Point out each leukocyte.
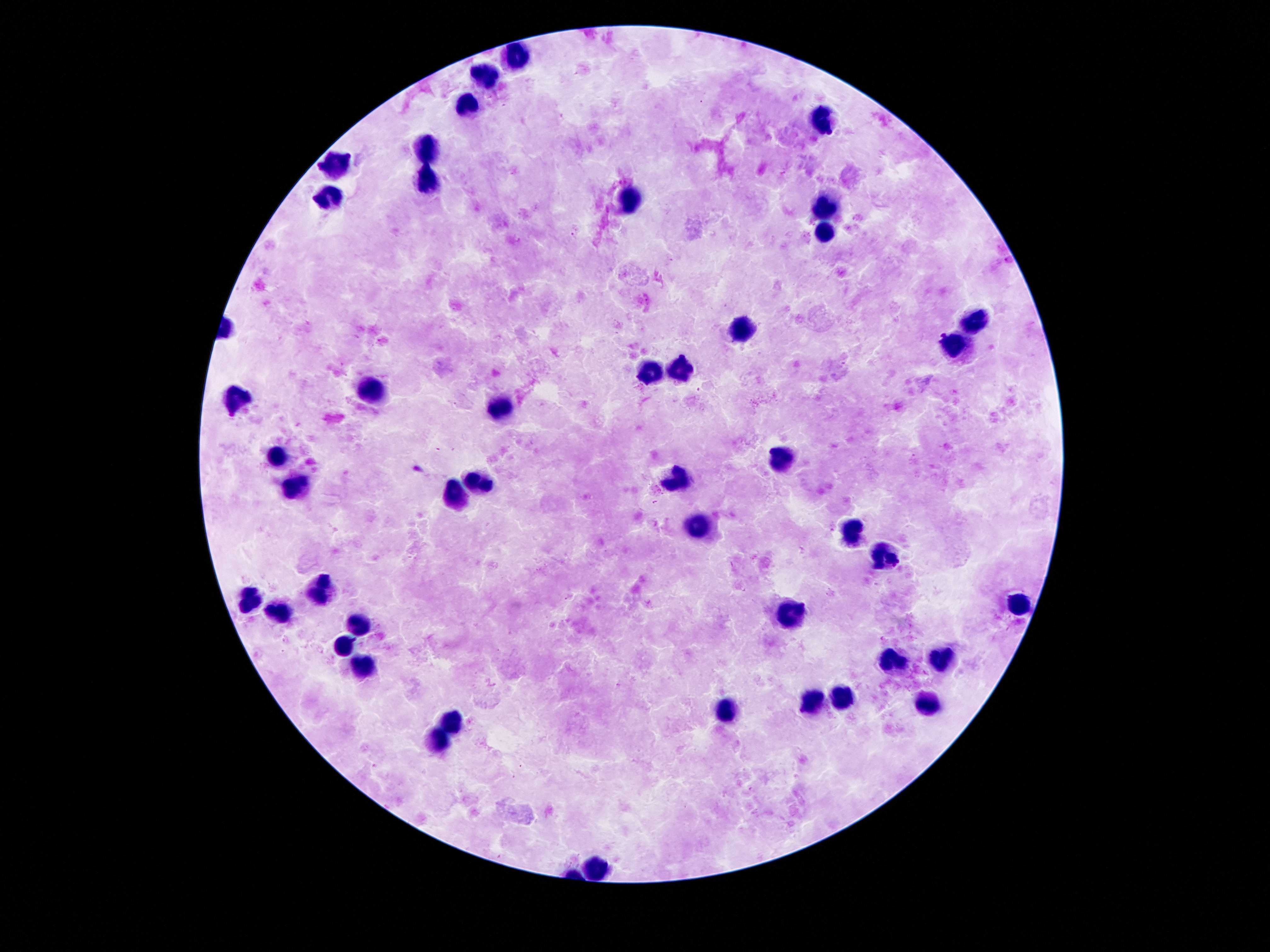
Approximate object centers, in pixels from the top-left corner.
Leukocytes: (x=511, y=58), (x=483, y=74), (x=466, y=105), (x=821, y=116), (x=425, y=146), (x=333, y=165), (x=429, y=179), (x=329, y=193), (x=630, y=197), (x=823, y=206), (x=827, y=234), (x=974, y=320), (x=741, y=331), (x=952, y=343), (x=683, y=365), (x=649, y=374), (x=372, y=390), (x=239, y=398), (x=499, y=410), (x=780, y=454), (x=280, y=456), (x=681, y=478), (x=481, y=482), (x=300, y=488), (x=454, y=495), (x=698, y=527), (x=851, y=531), (x=888, y=552), (x=321, y=587), (x=251, y=597), (x=1015, y=603), (x=284, y=611), (x=788, y=615), (x=360, y=622), (x=345, y=644), (x=935, y=656), (x=894, y=662), (x=364, y=665), (x=841, y=699), (x=812, y=701), (x=925, y=703), (x=728, y=712), (x=450, y=720), (x=440, y=742), (x=599, y=867).

Summary:
  - Stain: Giemsa
  - Patient malaria status: uninfected
  - Magnification: 100x
  - Capture: smartphone camera through the microscope eyepiece
  - Preparation: thick peripheral-blood smear
  - Image size: 1270×952 pixels
  - Field of view: one from this slide